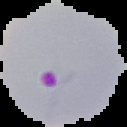
result = Plasmodium parasites identified
preparation = thin blood smear
image size = 127×127 pixels
image type = segmented cell region on a black background